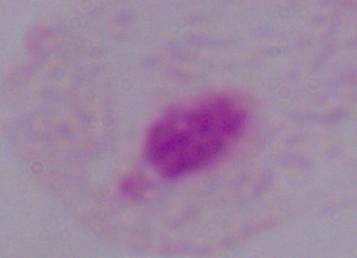 Micrograph. Captured at 1000x magnification. A trichomonad is shown.